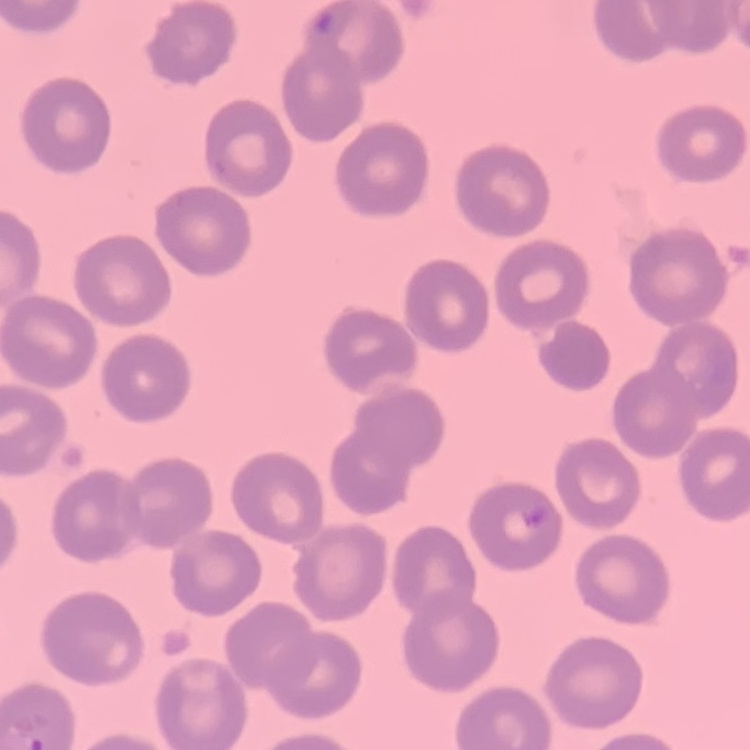
The red blood cells exhibit no rouleaux formation. Square crop of a larger photomicrograph. Thin peripheral smear. Field's or Giemsa stain.